Assess this cell for malaria.
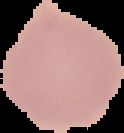

Uninfected.

image_size: 124×133 pixels
image_type: cell region segmented out of the field of view; surrounding area masked to black
preparation: thin blood smear